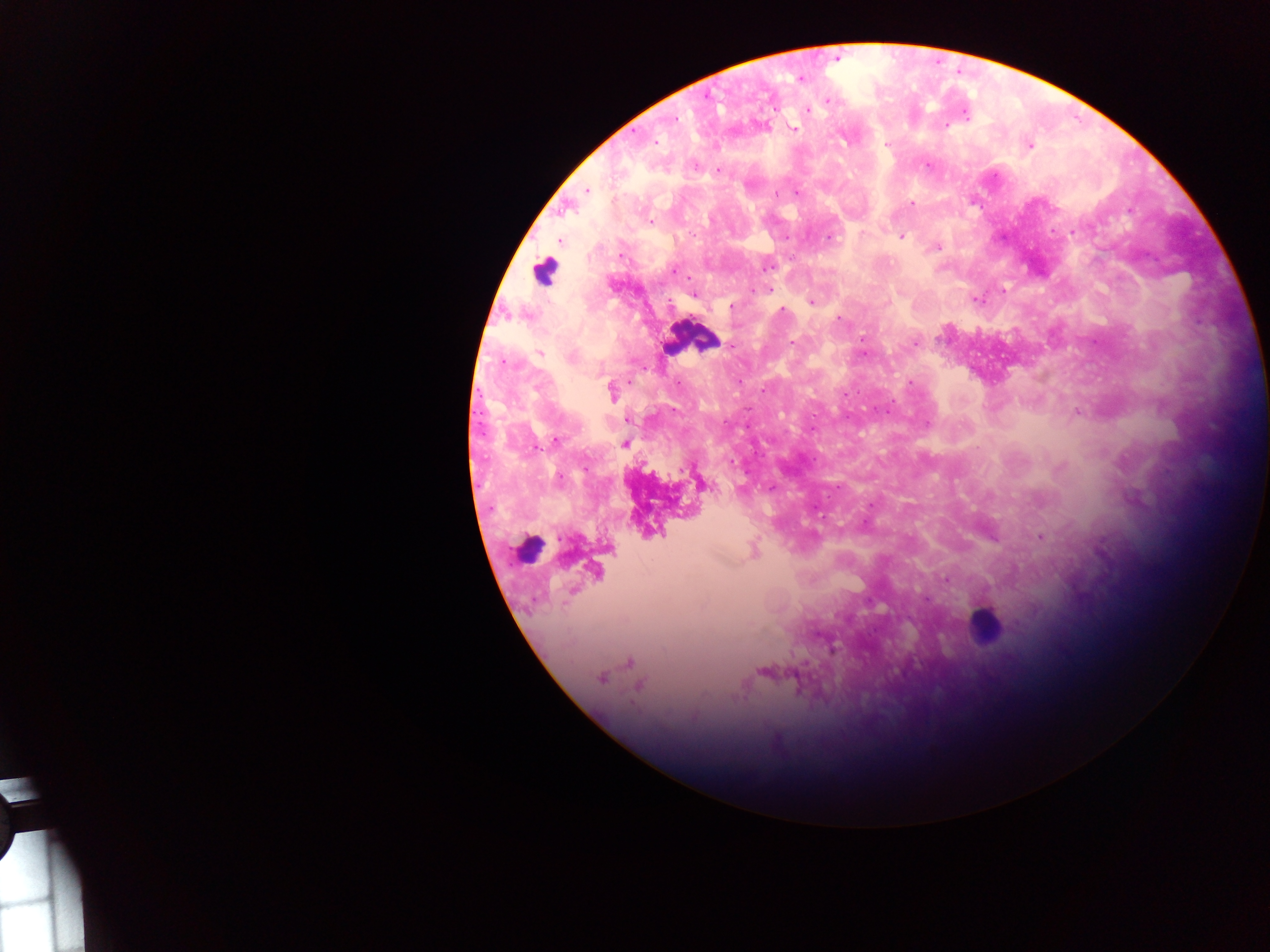

Approximate centers as (x, y) in pixels. Malaria parasite locations: (800, 78), (828, 100), (808, 110), (966, 115), (675, 120), (947, 125), (794, 129), (656, 142), (886, 145), (1029, 145), (927, 165), (695, 166), (718, 171), (587, 190), (796, 193), (776, 194), (912, 205), (1129, 210), (650, 222), (1072, 231), (862, 233), (901, 236), (829, 237), (786, 238), (559, 241), (938, 247), (622, 255), (767, 267), (673, 270), (752, 289), (768, 290), (1004, 290), (693, 296), (977, 300), (670, 302), (811, 303), (890, 303), (731, 307), (783, 309), (838, 318), (861, 338), (793, 343), (915, 343), (731, 346), (864, 352), (539, 353), (572, 358), (740, 382), (910, 383), (763, 389), (611, 392), (845, 394), (675, 411), (889, 411), (1077, 412), (627, 420), (725, 422), (927, 424), (556, 440), (624, 443), (731, 463), (585, 469), (1058, 469), (560, 479), (707, 486), (771, 487), (870, 505), (1040, 537), (946, 580), (601, 679). Leukocyte locations: (543, 273), (692, 337), (526, 548), (984, 624). Sample from Ghana. One field of view. Image is 1270×952 pixels. Mobile-phone photograph taken through the microscope. Thick blood smear.